Outline each blood parasite and name the species.
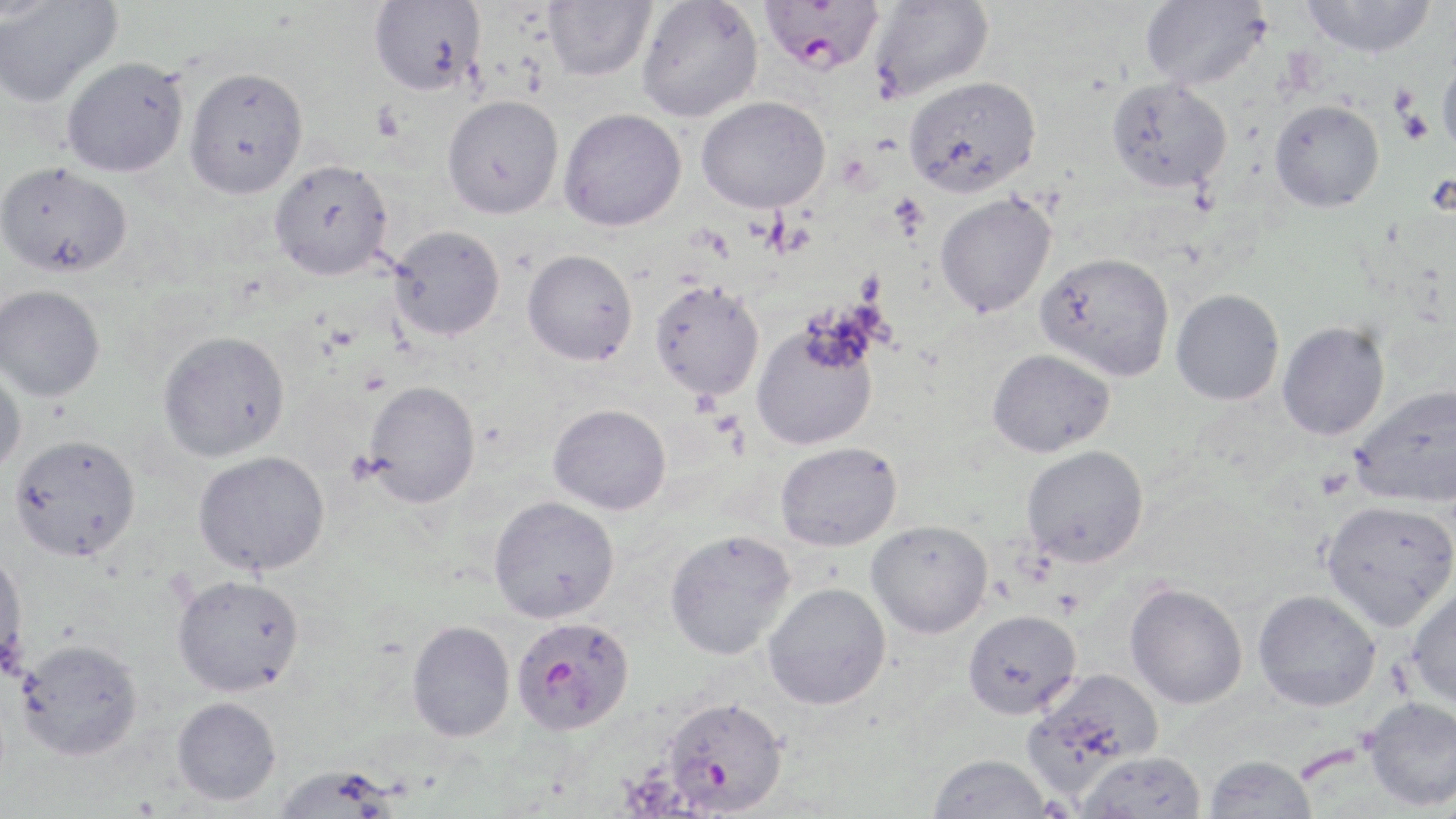
Approximate bounding boxes as (x1,y1)-(x2,y2) corner pairs in pixels.
Plasmodium falciparum-infected red blood cells: (758,0)-(885,74), (511,616)-(635,735), (662,696)-(788,815).
No Plasmodium ovale, Plasmodium malariae, Plasmodium vivax, Babesia divergens, or Trypanosoma brucei observed.

Platelet locations: (1397,103)-(1433,146), (372,104)-(405,142), (1315,468)-(1353,499). Uninfected red blood cell locations: (368,0)-(485,96), (543,0)-(656,81), (636,0)-(763,122), (869,0)-(994,102), (1139,0)-(1271,90), (1301,0)-(1437,58), (0,2)-(122,108), (1437,53)-(1456,159), (61,57)-(189,178), (183,66)-(308,199), (902,75)-(1041,199), (1106,77)-(1232,193), (442,94)-(564,219), (696,95)-(830,213), (1269,100)-(1384,212), (558,107)-(687,231), (269,159)-(394,281), (0,162)-(132,278), (934,192)-(1056,317), (388,225)-(505,340), (522,249)-(638,365), (1036,251)-(1175,381), (649,279)-(765,400), (0,284)-(105,401), (1170,289)-(1284,406), (1277,321)-(1390,440), (751,323)-(878,451), (157,330)-(289,462), (987,348)-(1114,458), (0,362)-(27,478), (364,380)-(481,507), (1351,384)-(1456,507), (548,403)-(671,515), (9,433)-(141,561), (775,441)-(902,551), (1021,445)-(1149,567), (193,450)-(330,575), (488,496)-(619,623), (1321,499)-(1456,630), (867,520)-(992,638), (664,529)-(796,660), (0,548)-(28,675), (171,573)-(305,697), (1407,581)-(1456,711), (763,582)-(891,710), (1125,582)-(1248,709), (1253,590)-(1381,711), (962,608)-(1082,719), (406,619)-(515,742), (16,638)-(143,761), (1023,667)-(1164,795), (172,696)-(281,806), (1364,697)-(1456,810), (1074,750)-(1207,818), (926,754)-(1053,818), (1203,754)-(1317,818), (271,764)-(402,818). Slide-level diagnosis: Plasmodium falciparum. Light microscopy. May-Grünwald-Giemsa-stained preparation. 1000x magnification. Single field of view. Image is 1456×819 pixels. Thin blood film.